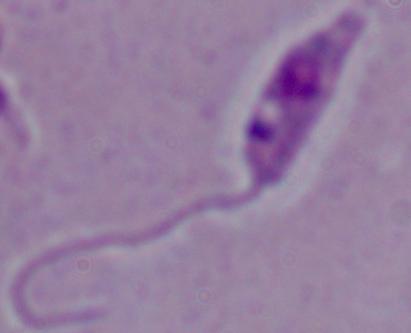
{
  "identification": "Leishmania",
  "magnification": "1000x",
  "modality": "micrograph"
}